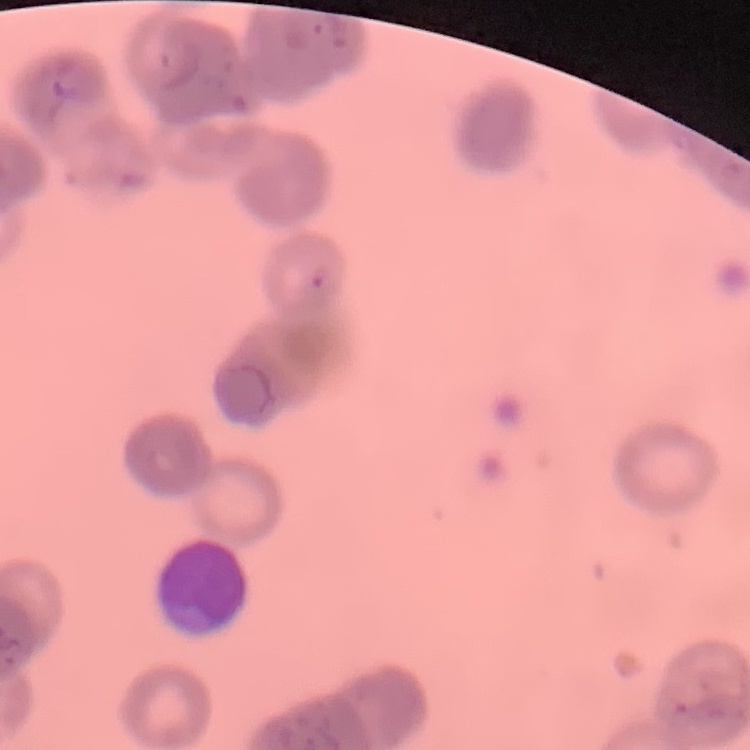

The red blood cells show rouleaux formation. Stained with either Field's or Giemsa. Thin blood smear. One tile cut from a larger photomicrograph.